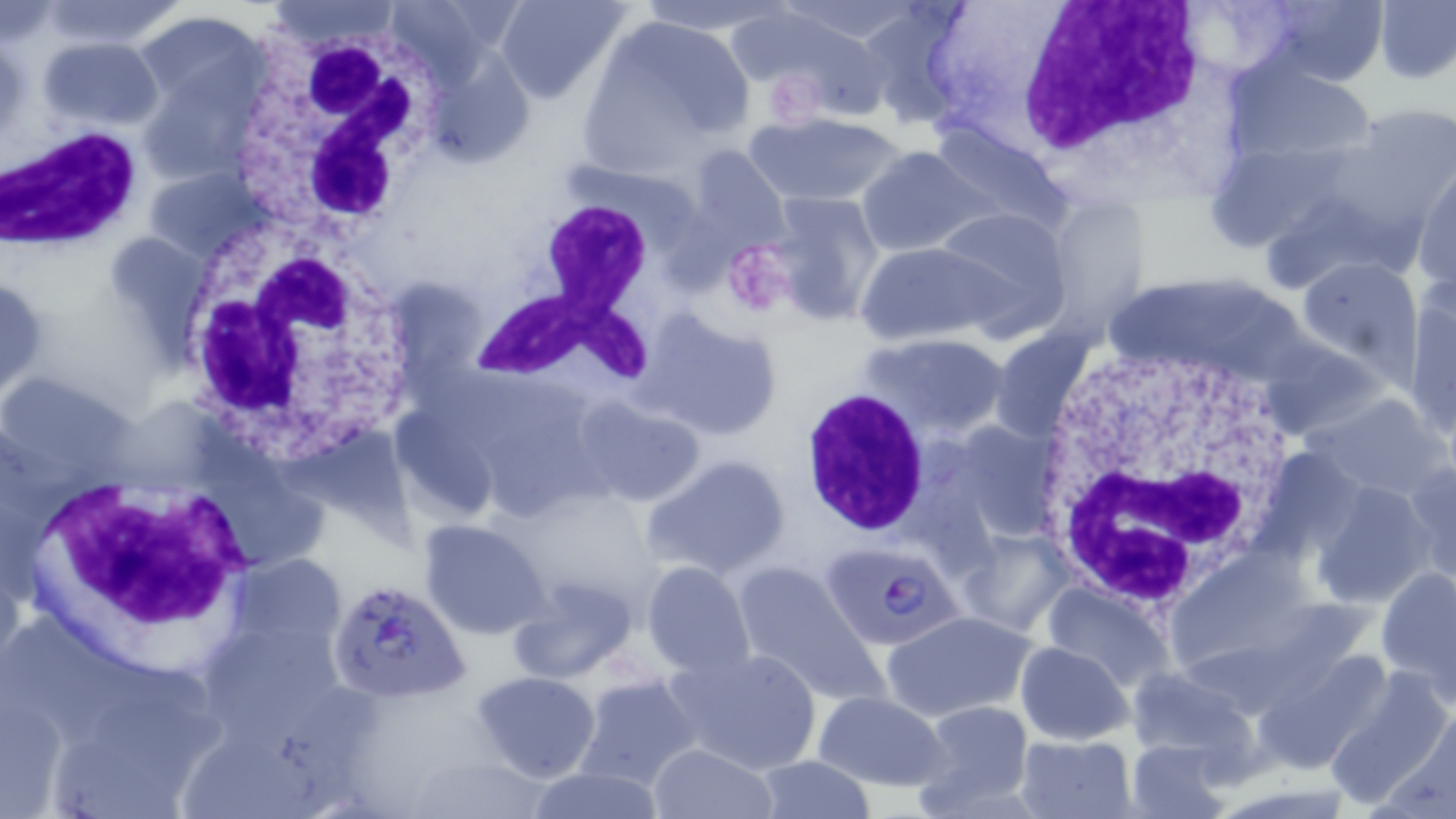
Approximate bounding boxes as (x1, y1, x2, y2) in pixels. Plasmodium falciparum-infected red blood cell locations: (820, 546, 970, 652), (329, 576, 468, 705). White blood cell locations: (1003, 3, 1216, 165), (241, 29, 435, 241), (0, 124, 143, 252), (470, 200, 667, 387), (175, 225, 417, 458), (1024, 336, 1304, 609), (797, 386, 931, 539), (32, 475, 255, 646). Uninfected red blood cell locations: (37, 0, 186, 50), (496, 0, 630, 105), (631, 0, 787, 37), (1258, 0, 1388, 88), (1375, 0, 1454, 84), (1183, 1, 1304, 86), (855, 2, 976, 124), (720, 6, 855, 97), (133, 11, 273, 123), (581, 13, 755, 164), (777, 24, 892, 123), (38, 36, 164, 130), (1228, 59, 1380, 164), (137, 73, 256, 187), (1337, 103, 1456, 228), (741, 111, 911, 208), (925, 120, 1070, 231), (1201, 138, 1358, 252), (680, 144, 791, 255), (857, 147, 989, 257), (145, 165, 267, 262), (1412, 165, 1456, 297), (760, 191, 885, 326), (1043, 194, 1151, 325), (933, 204, 1073, 339), (102, 231, 207, 333), (855, 242, 998, 345), (1296, 254, 1422, 373), (1402, 282, 1456, 439), (647, 314, 782, 441), (991, 328, 1094, 436), (862, 333, 1010, 436), (1256, 336, 1388, 441), (1303, 392, 1452, 502), (575, 396, 706, 507), (389, 406, 501, 526), (939, 418, 1066, 546), (1254, 445, 1368, 562), (642, 453, 791, 581), (1404, 457, 1456, 586), (1309, 481, 1436, 610), (417, 517, 554, 641), (957, 529, 1075, 638), (228, 552, 349, 649), (641, 560, 756, 677), (732, 563, 883, 703), (1376, 565, 1455, 697), (505, 576, 640, 684), (1043, 582, 1173, 695), (881, 610, 1036, 723), (197, 615, 347, 741), (1015, 641, 1133, 745), (664, 646, 824, 774), (1251, 650, 1391, 774), (1122, 666, 1255, 770), (1327, 668, 1456, 810), (471, 669, 600, 783), (573, 672, 702, 792), (2, 687, 68, 816), (812, 691, 950, 791), (912, 700, 1034, 813), (1014, 733, 1135, 819), (1127, 738, 1233, 819), (649, 743, 776, 819), (402, 750, 550, 818), (754, 757, 875, 817), (522, 768, 662, 819). Platelet locations: (724, 239, 793, 320). Slide-level diagnosis: Plasmodium falciparum. Thin blood smear. May-Grünwald-Giemsa stain. One field of a larger specimen. Captured at 1000x magnification. Image is 1456×819 pixels. Light microscopy.